Give the position of every leukocyte visible.
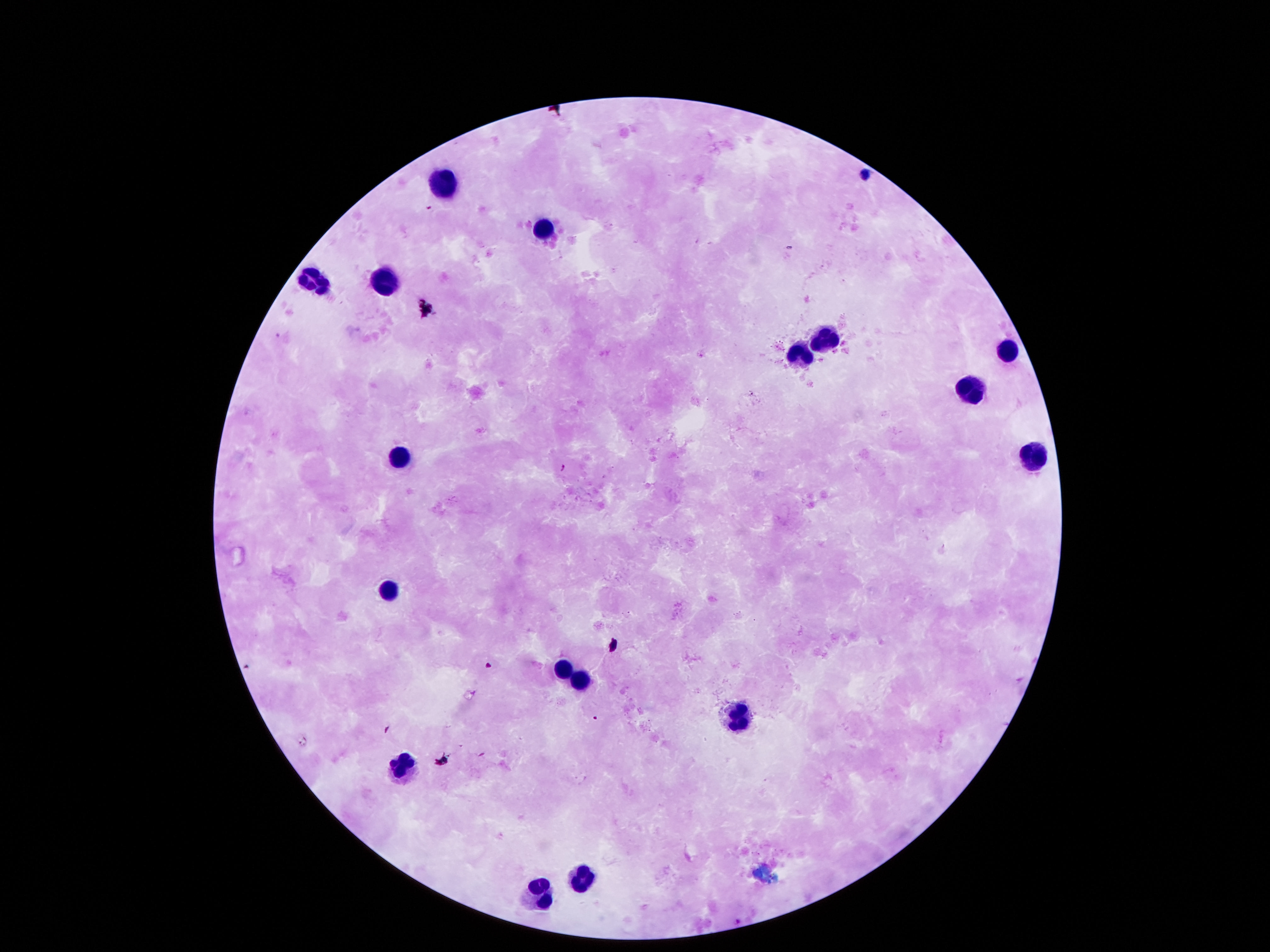

Approximate centers as (x, y) in pixels.
Leukocytes: (440, 184), (541, 226), (314, 280), (385, 281), (825, 338), (1006, 349), (799, 352), (970, 387), (1035, 454), (395, 462), (389, 590), (566, 665), (583, 678), (734, 716), (405, 767), (579, 875), (528, 901).

Single field of view. Smartphone photograph taken through the microscope eyepiece. Giemsa stain. Thick blood smear. Image is 1270×952 pixels. 100x magnification. Patient malaria status: uninfected.